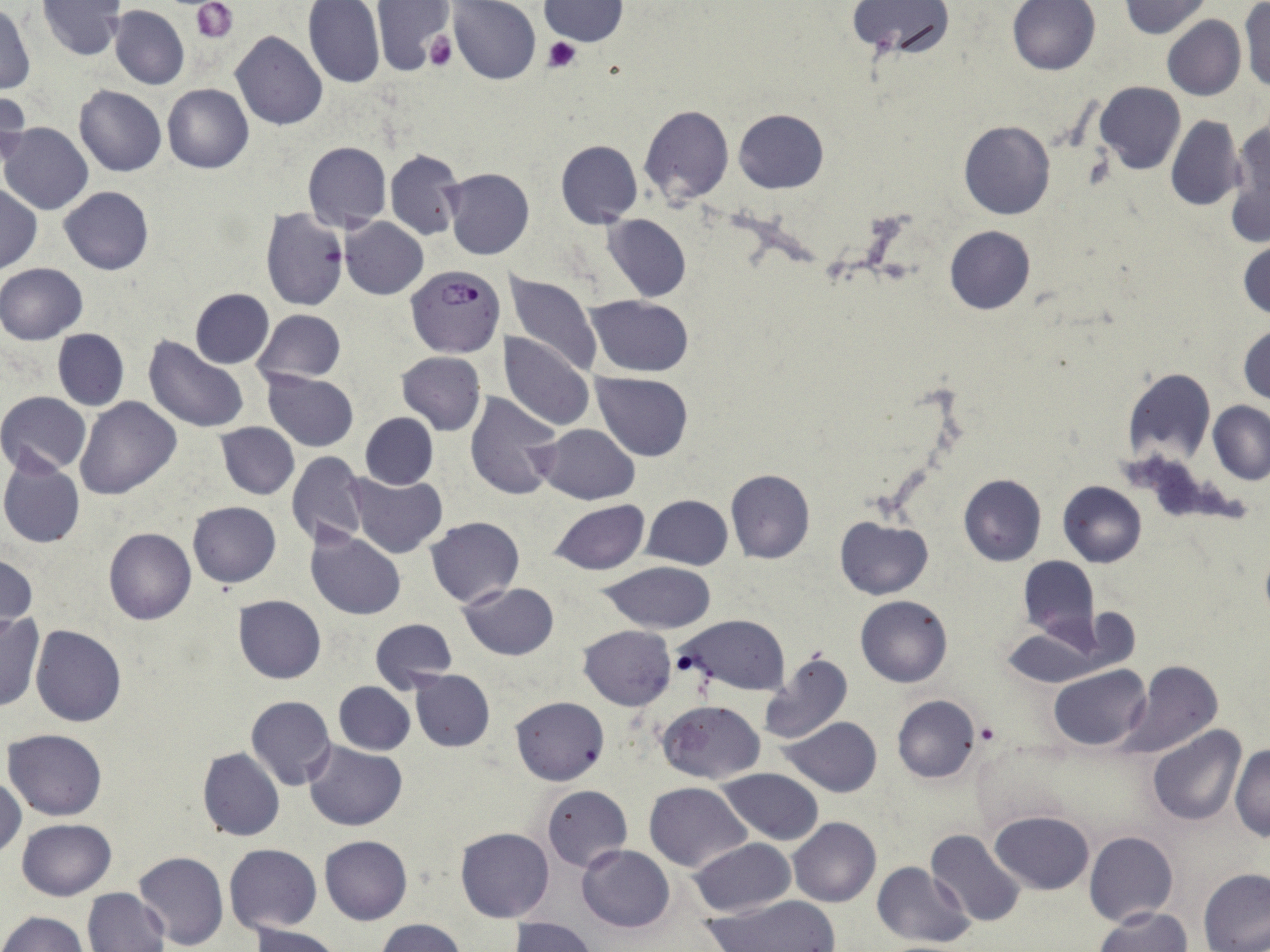
Approximate bounding boxes as (x1,y1)-(x2,y2) corner pairs in pixels. Platelet locations: (192,2)-(238,42), (424,30)-(456,71), (542,36)-(580,74), (974,721)-(1002,747). Plasmodium falciparum-infected red blood cell locations: (406,265)-(503,357). Uninfected red blood cell locations: (37,0)-(127,61), (370,0)-(455,76), (447,0)-(541,85), (847,0)-(955,61), (1008,0)-(1099,75), (303,1)-(385,88), (540,1)-(627,46), (1122,1)-(1209,39), (1240,1)-(1269,92), (0,5)-(36,96), (109,5)-(189,90), (1162,15)-(1245,101), (231,31)-(327,131), (1095,82)-(1186,174), (162,84)-(253,173), (75,86)-(166,177), (0,90)-(29,171), (639,105)-(734,207), (734,109)-(828,193), (1165,114)-(1246,211), (1224,118)-(1270,248), (958,121)-(1055,220), (1,123)-(93,215), (556,140)-(642,228), (302,141)-(391,232), (385,147)-(464,240), (443,168)-(533,260), (1,185)-(41,272), (59,185)-(154,275), (261,208)-(349,309), (603,213)-(691,302), (339,217)-(428,299), (945,225)-(1034,314), (1239,240)-(1269,321), (0,262)-(88,344), (501,271)-(603,379), (189,288)-(274,368), (587,296)-(694,377), (253,309)-(345,385), (1238,323)-(1269,407), (52,329)-(128,410), (499,333)-(594,432), (143,336)-(252,434), (397,352)-(486,434), (1120,367)-(1216,468), (264,370)-(358,450), (591,372)-(695,461), (0,391)-(90,475), (465,391)-(563,499), (75,396)-(183,500), (1209,401)-(1270,484), (360,413)-(438,489), (217,422)-(298,500), (535,424)-(638,504), (286,451)-(369,548), (0,455)-(86,549), (725,468)-(816,563), (345,472)-(447,558), (959,474)-(1046,566), (1058,480)-(1147,567), (641,495)-(732,570), (548,500)-(649,575), (188,501)-(281,587), (425,516)-(523,607), (835,516)-(933,599), (306,527)-(405,620), (104,528)-(195,624), (0,552)-(37,634), (1019,557)-(1098,642), (598,562)-(719,634), (460,582)-(559,660), (855,594)-(953,686), (233,595)-(327,683), (0,611)-(44,711), (677,614)-(789,695), (369,618)-(456,692), (579,625)-(676,710), (30,626)-(126,727), (1001,626)-(1104,687), (757,650)-(854,745), (1119,660)-(1223,760), (1050,665)-(1150,751), (410,670)-(495,752), (334,682)-(415,755), (246,695)-(335,790), (891,695)-(981,784), (510,697)-(609,786), (658,700)-(766,784), (784,717)-(883,796), (1147,726)-(1246,824), (4,728)-(108,820), (304,740)-(408,831), (1230,745)-(1270,842), (198,747)-(285,841), (716,768)-(824,843), (1,772)-(24,860), (643,781)-(752,872), (542,785)-(632,870), (990,810)-(1096,894), (788,817)-(881,907), (17,818)-(115,901), (455,827)-(554,923), (926,829)-(1028,928), (1084,831)-(1178,927), (320,836)-(412,925), (688,838)-(794,917), (223,844)-(322,934), (578,844)-(675,931), (133,851)-(228,950), (870,861)-(975,948), (1198,867)-(1270,951), (83,887)-(171,951), (702,896)-(841,952), (1095,907)-(1192,952), (2,911)-(89,952), (512,917)-(595,952), (376,918)-(468,951), (248,924)-(344,952). Slide-level diagnosis: Plasmodium falciparum. One field of a larger specimen. May-Grünwald-Giemsa stain. Image is 1270×952 pixels. Thin blood smear. Optical microscopy. 1000x magnification.